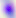
{
  "identification": "Toxoplasma gondii",
  "magnification": "400x",
  "modality": "micrograph"
}